State the blood parasite species.
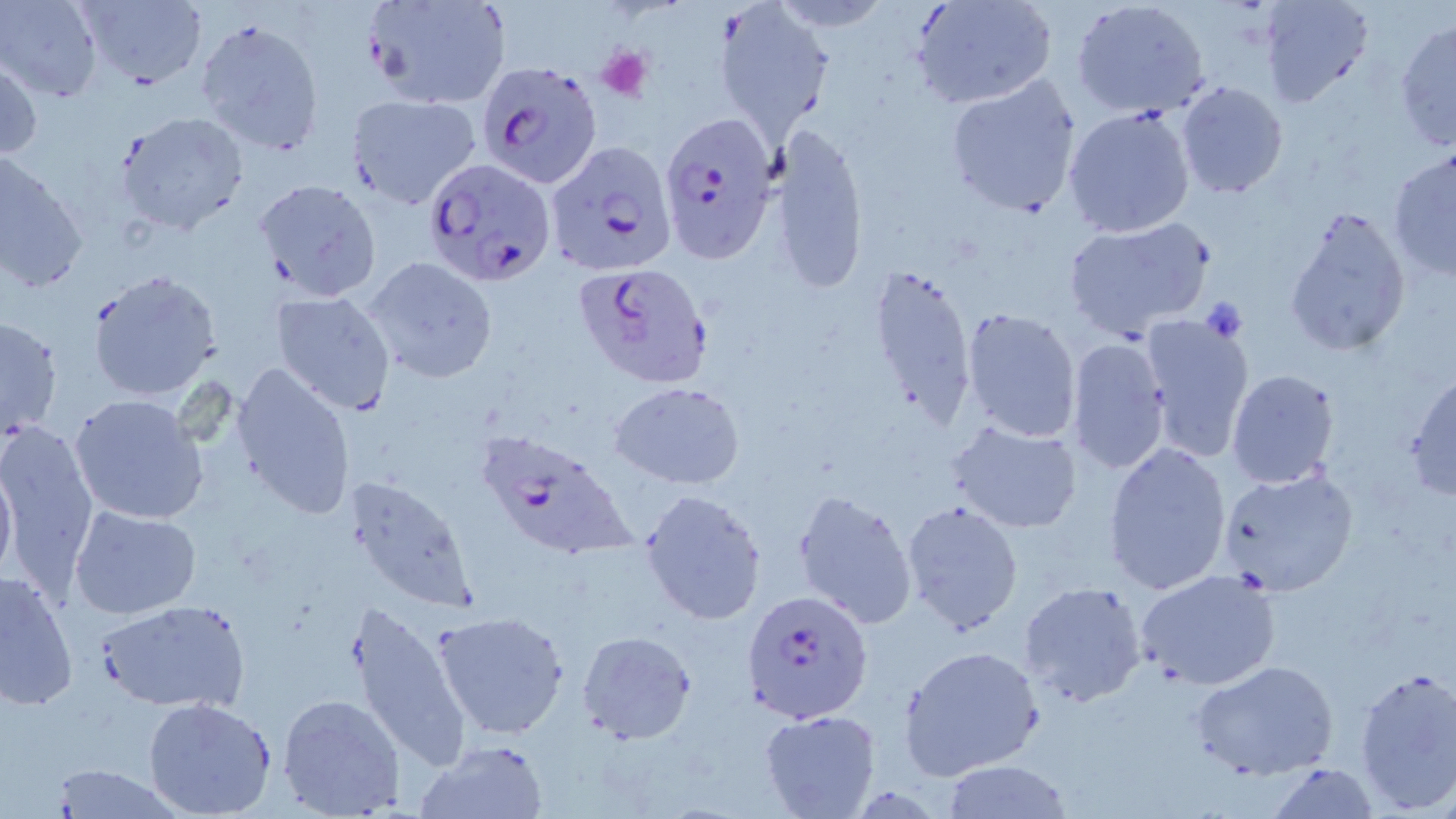

Plasmodium falciparum.

Summary:
  - Coordinate format: approximate bounding boxes as (x1, y1, x2, y2) in pixels
  - Uninfected red blood cell locations: (1, 0, 103, 102), (70, 0, 208, 91), (359, 0, 513, 109), (910, 0, 1060, 111), (1071, 0, 1211, 119), (1257, 0, 1373, 108), (717, 7, 831, 136), (1394, 17, 1456, 155), (194, 18, 327, 156), (0, 58, 42, 163), (944, 73, 1083, 219), (1176, 81, 1289, 200), (345, 92, 482, 209), (1062, 104, 1197, 238), (114, 110, 250, 237), (768, 126, 870, 295), (1387, 150, 1456, 282), (0, 156, 88, 295), (255, 177, 383, 300), (1282, 203, 1413, 359), (1062, 216, 1217, 341), (363, 257, 497, 383), (867, 261, 978, 434), (87, 271, 221, 401), (272, 289, 397, 415), (960, 306, 1083, 443), (1135, 311, 1255, 460), (0, 316, 63, 441), (1066, 338, 1171, 475), (231, 361, 356, 519), (1225, 368, 1341, 490), (1403, 368, 1456, 502), (610, 381, 745, 488), (69, 392, 209, 524), (0, 418, 101, 593), (930, 419, 1060, 625), (946, 420, 1082, 533), (1102, 442, 1233, 595), (0, 456, 17, 587), (1216, 465, 1361, 596), (345, 476, 479, 612), (639, 488, 768, 626), (793, 488, 917, 629), (900, 500, 1024, 636), (69, 505, 202, 619), (1135, 568, 1284, 692), (1, 571, 77, 710), (1017, 579, 1147, 708), (342, 598, 474, 773), (96, 599, 250, 712), (433, 608, 569, 739), (577, 631, 697, 743), (898, 644, 1044, 778), (1191, 659, 1340, 781), (1354, 665, 1456, 812), (277, 691, 405, 818), (141, 696, 278, 818), (760, 711, 882, 819), (414, 739, 548, 818), (938, 760, 1076, 817), (1266, 763, 1381, 819), (47, 764, 183, 819)
  - Platelet locations: (595, 46, 653, 102), (1198, 298, 1247, 342)
  - Plasmodium falciparum-infected red blood cell locations: (473, 61, 598, 190), (656, 111, 775, 265), (543, 139, 677, 276), (422, 158, 555, 285), (576, 263, 715, 389), (472, 427, 638, 559), (743, 590, 874, 723)
  - Field of view: one of a larger specimen
  - Magnification: 1000x
  - Image size: 1456×819 pixels
  - Modality: optical microscopy
  - Stain: May-Grünwald-Giemsa
  - Preparation: thin blood film